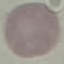

{
  "result": "no malaria parasites seen",
  "stain": "Giemsa",
  "capture": "smartphone camera at the microscope eyepiece",
  "image_type": "cell patch, automatically extracted from a larger field of view and resized to 64 × 64 pixels",
  "preparation": "thin blood film"
}